Assess this cell for malaria.
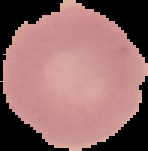

Uninfected.

{
  "image_size": "148×151 pixels",
  "preparation": "thin blood film",
  "image_type": "segmented cell region on a black background"
}